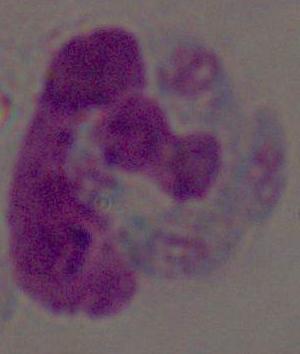
{
  "modality": "photomicrograph",
  "magnification": "1000x",
  "identification": "white blood cell"
}